Assess this cell for malaria.
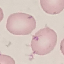
Uninfected.

Giemsa stain. Photographed with a smartphone camera at the microscope eyepiece. Automatically extracted cell patch, resized to 64 × 64 pixels. Thin blood film.